Classify this cell by malaria status.
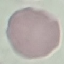

Uninfected.

Summary:
  - Capture: smartphone camera at the microscope eyepiece
  - Image type: automatically extracted cell patch, resized to 64 × 64 pixels
  - Stain: Giemsa
  - Preparation: thin smear